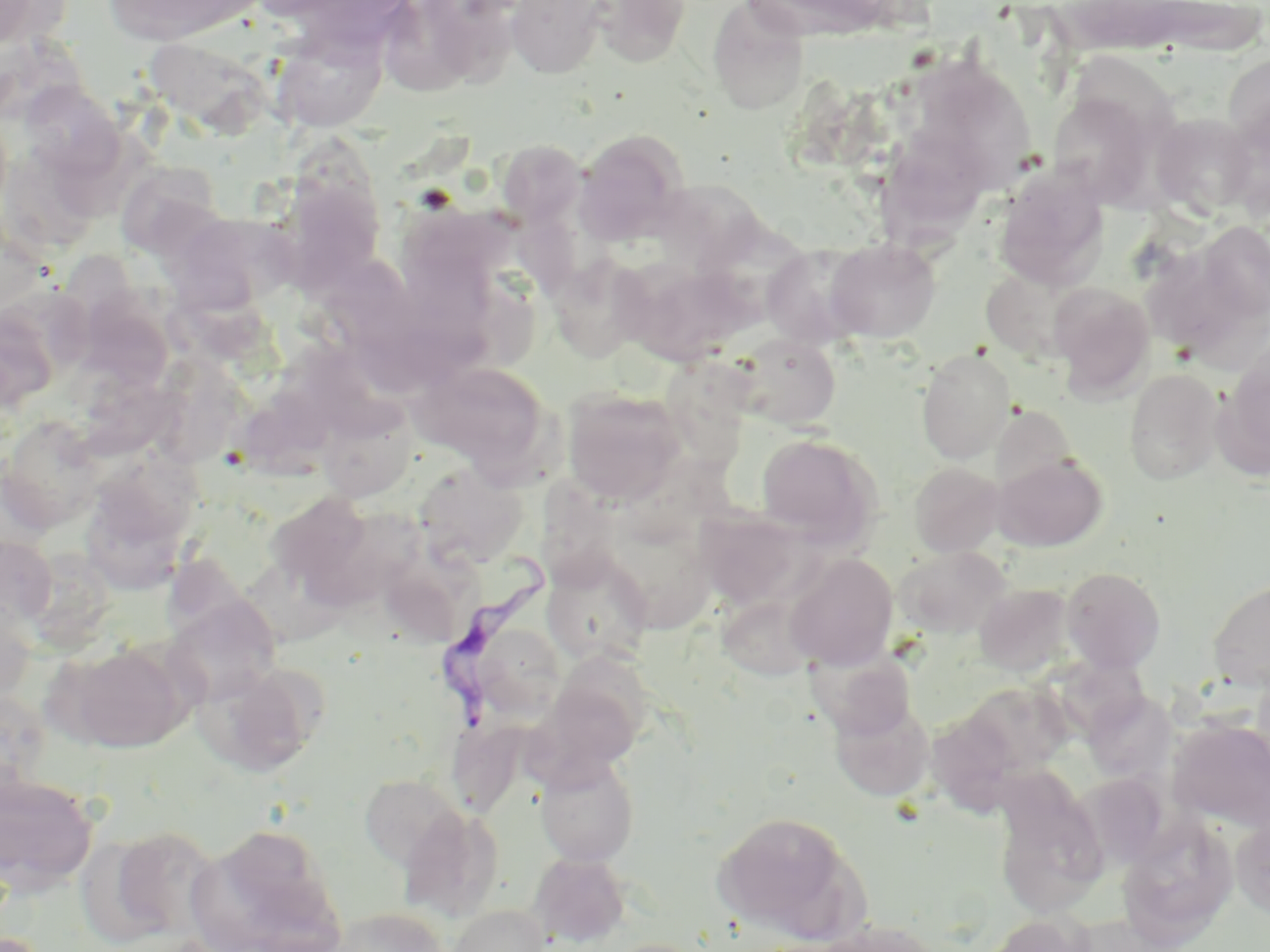
slide_level_diagnosis: Trypanosoma brucei
preparation: thin blood smear
image_size: 1270×952 pixels
uninfected_red_blood_cell_locations: 'approximate bounding boxes as (x1, y1, x2, y2) in pixels: (104, 0, 262, 46), (277, 0, 421, 50), (421, 0, 520, 94), (505, 0, 609, 79), (589, 0, 692, 67), (744, 0, 896, 41), (1134, 0, 1270, 58), (0, 1, 63, 54), (707, 2, 809, 114), (270, 25, 388, 133), (1223, 53, 1270, 159), (913, 59, 1038, 195), (18, 81, 124, 179), (1048, 90, 1162, 208), (1150, 114, 1257, 218), (573, 129, 690, 243), (496, 139, 585, 227), (878, 140, 993, 261), (114, 161, 224, 258), (994, 166, 1110, 291), (277, 177, 385, 292), (174, 211, 298, 312), (1196, 222, 1270, 323), (825, 238, 941, 342), (761, 244, 873, 348), (548, 254, 654, 363), (325, 258, 424, 353), (618, 259, 750, 365), (981, 264, 1093, 365), (1049, 283, 1156, 402), (730, 334, 842, 431), (1221, 346, 1270, 476), (916, 348, 1016, 463), (412, 360, 552, 474), (1124, 368, 1224, 485), (562, 388, 689, 505), (317, 398, 417, 502), (990, 405, 1079, 499), (1, 415, 105, 532), (755, 433, 880, 546), (94, 451, 205, 539), (992, 453, 1108, 552), (413, 462, 528, 570), (909, 462, 1006, 558), (265, 491, 375, 593), (701, 494, 813, 613), (83, 507, 197, 596), (609, 528, 723, 633), (0, 534, 58, 631), (894, 545, 1011, 638), (542, 549, 654, 668), (784, 553, 899, 671), (1061, 566, 1166, 674), (1207, 578, 1270, 690), (974, 582, 1075, 677), (717, 593, 818, 681), (163, 595, 282, 706), (0, 600, 37, 705), (57, 642, 190, 753), (805, 642, 918, 745), (196, 664, 322, 777), (540, 673, 647, 775), (0, 689, 52, 802), (965, 689, 1070, 783), (1083, 689, 1174, 781), (829, 695, 935, 802), (935, 716, 1024, 820), (1169, 719, 1270, 832), (535, 754, 639, 866), (0, 771, 99, 894), (1073, 771, 1170, 869), (359, 773, 466, 869), (992, 778, 1108, 918), (399, 807, 504, 921), (710, 810, 866, 941), (1117, 813, 1238, 946), (1231, 815, 1270, 919), (104, 824, 220, 941), (187, 825, 344, 952), (527, 851, 631, 947), (448, 904, 550, 952), (332, 906, 448, 952), (980, 913, 1095, 952), (810, 919, 942, 952), (598, 938, 714, 952)'
trypanosoma_brucei_locations: 'approximate bounding boxes as (x1, y1, x2, y2) in pixels: (432, 545, 554, 743)'
magnification: 1000x
stain: May-Grünwald-Giemsa
field_of_view: single
modality: light microscopy